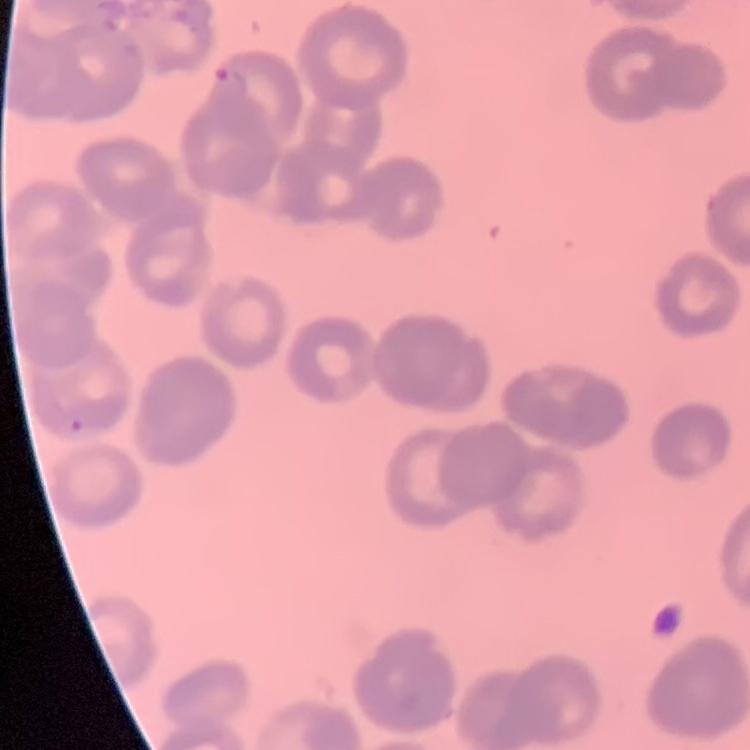
{
  "erythrocyte_morphology": "rouleaux formation",
  "preparation": "thin blood film",
  "image_type": "one tile cut from a larger photomicrograph",
  "stain": "Field's or Giemsa"
}